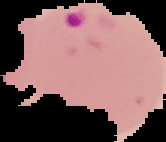 Malaria status: parasitized. Segmented cell region on a black background. From a thin blood film. Image is 166×142 pixels.